Identify the cell.
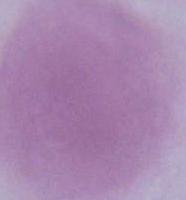
This is an erythrocyte.

Summary:
  - Modality: photomicrograph
  - Magnification: 1000x